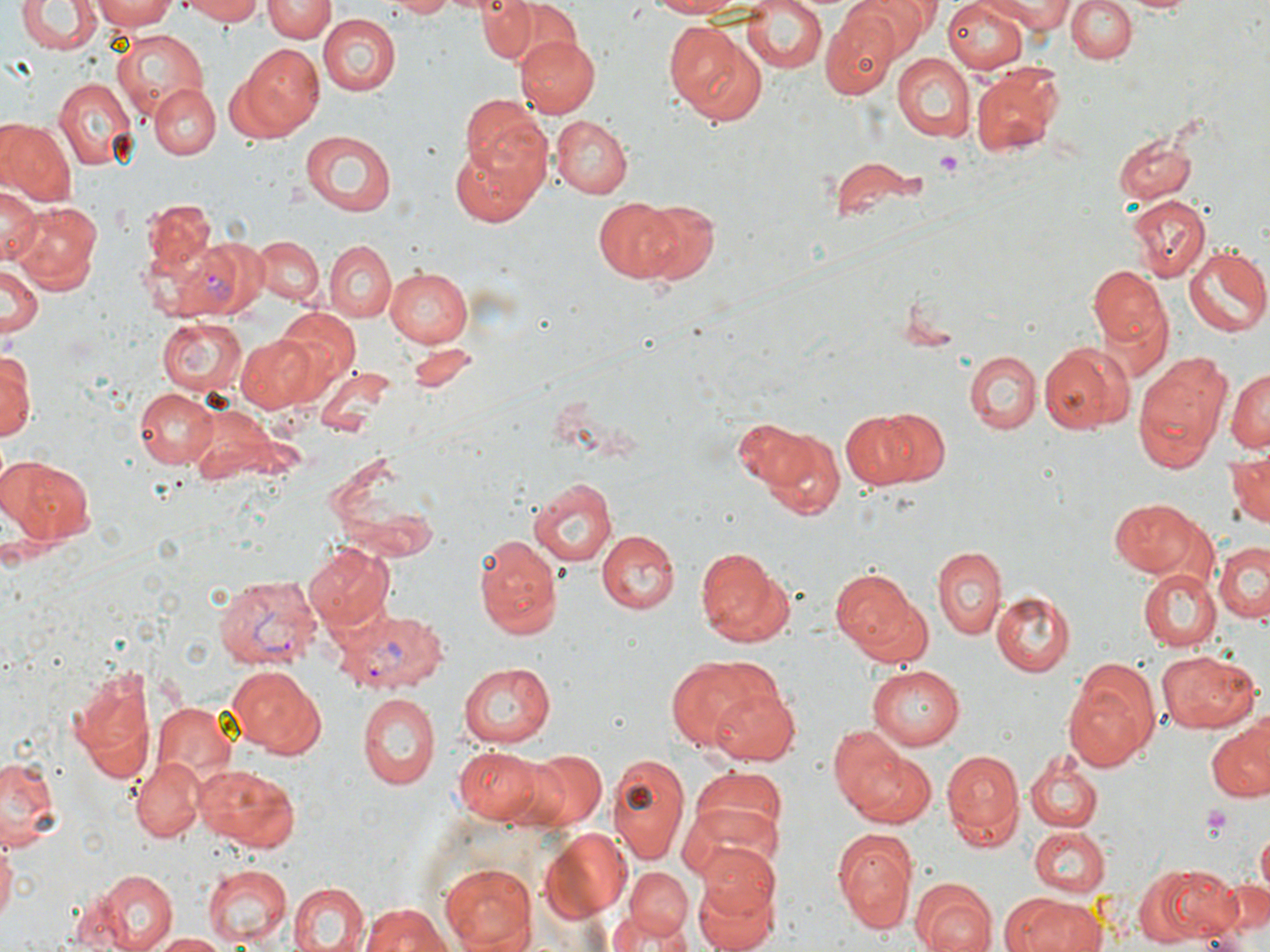
slide-level diagnosis = Plasmodium vivax
stain = May-Grünwald-Giemsa
magnification = 1000x
platelet locations = approximate bounding boxes as [x1, y1, x2, y2] in pixels: [936, 151, 964, 175], [1202, 803, 1236, 838]
uninfected red blood cell locations = approximate bounding boxes as [x1, y1, x2, y2] in pixels: [92, 0, 181, 30], [172, 0, 268, 23], [262, 0, 335, 43], [378, 0, 462, 18], [477, 0, 573, 66], [642, 0, 763, 19], [850, 0, 935, 52], [985, 0, 1072, 32], [1065, 0, 1138, 63], [16, 1, 101, 56], [943, 1, 1028, 73], [1122, 1, 1201, 16], [740, 2, 828, 76], [319, 14, 401, 96], [820, 15, 899, 102], [663, 22, 767, 126], [111, 28, 208, 116], [517, 35, 600, 116], [238, 45, 324, 134], [892, 54, 975, 141], [971, 68, 1060, 155], [53, 77, 136, 170], [150, 84, 219, 158], [459, 95, 553, 194], [550, 115, 634, 199], [1, 120, 76, 207], [300, 130, 399, 216], [1114, 132, 1197, 202], [451, 140, 543, 227], [827, 156, 928, 228], [0, 181, 41, 266], [1126, 195, 1209, 282], [142, 197, 217, 279], [593, 197, 681, 282], [629, 200, 721, 284], [11, 203, 103, 293], [252, 236, 323, 305], [325, 240, 395, 322], [1183, 244, 1269, 336], [3, 258, 42, 339], [1090, 266, 1172, 355], [387, 267, 474, 347], [265, 304, 359, 406], [158, 315, 248, 397], [235, 333, 321, 413], [1039, 343, 1129, 434], [3, 345, 35, 445], [965, 350, 1042, 435], [1134, 350, 1231, 472], [1227, 366, 1270, 456], [315, 367, 396, 440], [134, 388, 220, 470], [185, 407, 278, 484], [839, 410, 930, 489], [879, 410, 948, 485], [735, 419, 841, 514], [1225, 449, 1270, 530], [5, 459, 95, 543], [528, 475, 619, 566], [1107, 498, 1201, 576], [595, 530, 680, 614], [472, 533, 563, 643], [1214, 539, 1268, 623], [307, 543, 394, 632], [932, 545, 1006, 640], [693, 546, 793, 647], [833, 566, 926, 660], [1138, 568, 1221, 650], [991, 591, 1075, 676], [1159, 649, 1260, 733], [660, 655, 774, 752], [1065, 658, 1163, 768], [460, 662, 560, 749], [66, 663, 156, 786], [229, 664, 325, 757], [867, 666, 966, 749], [709, 684, 799, 766], [355, 691, 441, 793], [152, 700, 235, 785], [1206, 724, 1270, 803], [831, 725, 917, 820], [454, 745, 546, 821], [941, 747, 1024, 850], [517, 748, 607, 833], [0, 750, 62, 850], [607, 750, 691, 863], [1024, 750, 1104, 834], [131, 758, 204, 840], [194, 762, 300, 851], [688, 770, 787, 859], [679, 804, 781, 887], [832, 826, 916, 933], [1028, 827, 1110, 895], [540, 829, 630, 917], [0, 832, 17, 932], [693, 841, 781, 923], [436, 864, 537, 952], [1133, 864, 1239, 947], [202, 865, 292, 946], [624, 866, 695, 940], [89, 869, 178, 951], [692, 877, 782, 952], [1213, 877, 1270, 945], [288, 881, 369, 952], [912, 881, 996, 952], [1009, 894, 1103, 952], [359, 903, 455, 952], [615, 905, 688, 948], [148, 933, 232, 951]
image size = 1270×952 pixels
Plasmodium vivax-infected red blood cell locations = approximate bounding boxes as [x1, y1, x2, y2] in pixels: [159, 237, 269, 322], [214, 575, 321, 671], [334, 609, 450, 693]
modality = optical microscopy
field of view = single
preparation = thin blood smear